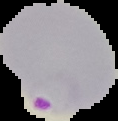

Segmented cell region on a black background. Malaria status: parasitized. Image is 118×121 pixels. From a thin blood film.